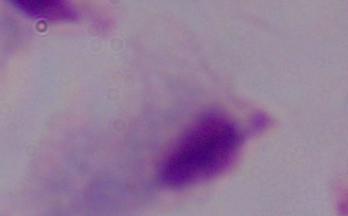
Summary:
  - Identification: trichomonad
  - Magnification: 1000x
  - Modality: photomicrograph